Point out each leukocyte.
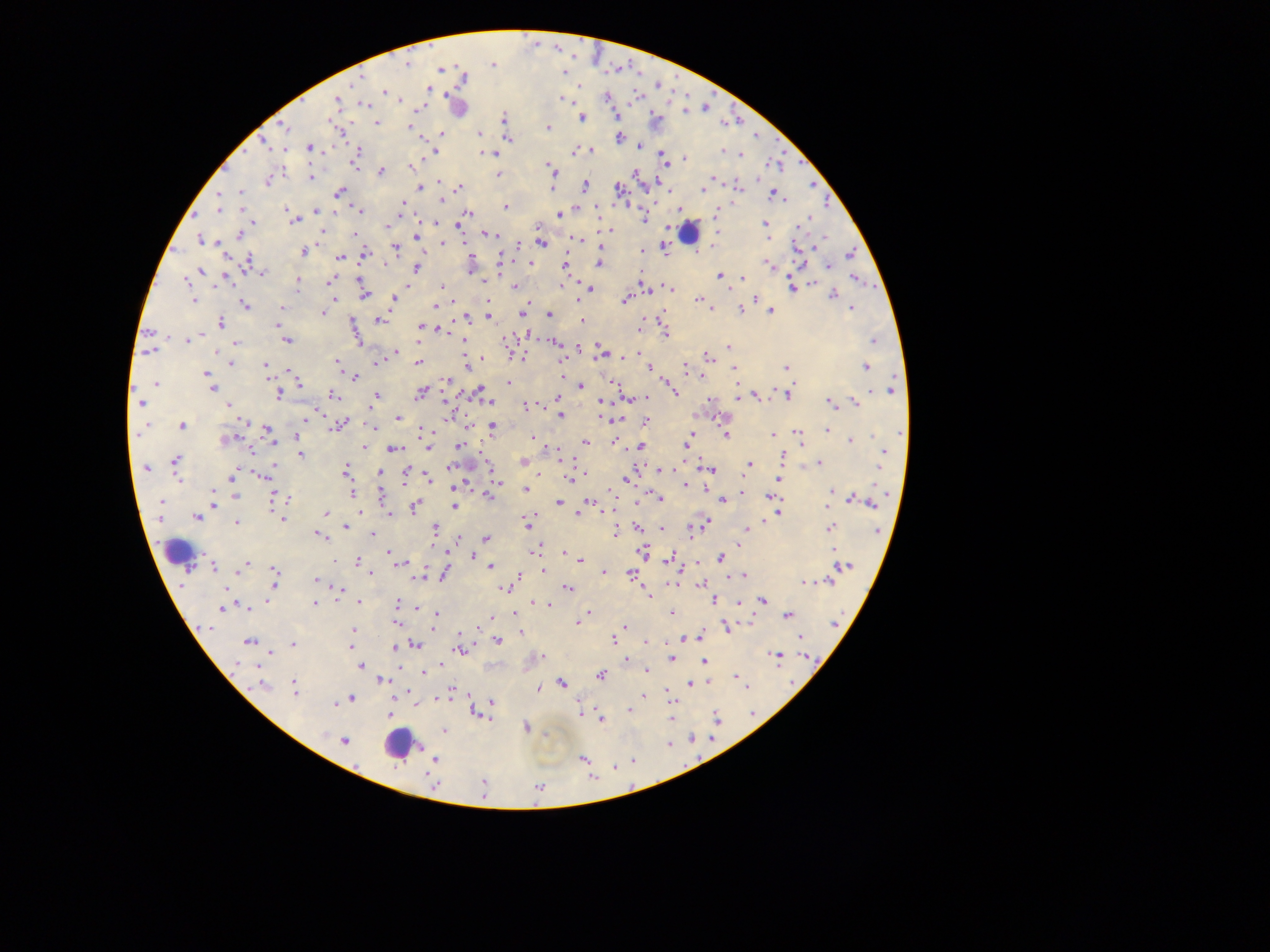

Approximate centers as {x, y} in pixels.
Leukocytes: {457, 106}, {688, 232}, {470, 462}, {178, 552}, {400, 744}.

Plasmodium parasite locations: {406, 62}, {493, 62}, {441, 68}, {564, 69}, {358, 77}, {428, 89}, {384, 91}, {566, 97}, {607, 97}, {642, 97}, {398, 100}, {337, 101}, {363, 104}, {684, 109}, {615, 116}, {503, 118}, {582, 118}, {328, 121}, {377, 122}, {409, 126}, {286, 128}, {548, 128}, {442, 134}, {479, 134}, {618, 138}, {508, 139}, {263, 142}, {640, 146}, {309, 147}, {358, 151}, {575, 151}, {590, 151}, {723, 151}, {434, 152}, {740, 153}, {493, 154}, {685, 158}, {663, 159}, {665, 163}, {355, 164}, {548, 165}, {551, 169}, {381, 171}, {497, 175}, {311, 177}, {267, 181}, {441, 182}, {813, 185}, {585, 186}, {737, 187}, {419, 188}, {459, 188}, {552, 188}, {619, 189}, {704, 190}, {240, 191}, {340, 192}, {776, 195}, {442, 200}, {401, 204}, {505, 207}, {220, 209}, {578, 209}, {316, 211}, {361, 211}, {715, 212}, {466, 214}, {560, 214}, {290, 215}, {464, 219}, {644, 219}, {294, 220}, {802, 223}, {458, 224}, {765, 224}, {387, 226}, {606, 230}, {321, 231}, {353, 233}, {239, 235}, {492, 235}, {417, 236}, {769, 238}, {201, 239}, {574, 240}, {466, 241}, {443, 243}, {520, 243}, {542, 243}, {601, 246}, {396, 249}, {665, 249}, {642, 251}, {303, 252}, {363, 254}, {850, 254}, {339, 257}, {248, 262}, {600, 263}, {530, 264}, {770, 264}, {564, 265}, {828, 266}, {417, 267}, {201, 271}, {469, 271}, {261, 273}, {720, 274}, {640, 277}, {743, 278}, {224, 279}, {856, 279}, {186, 281}, {330, 281}, {297, 282}, {359, 282}, {812, 284}, {217, 285}, {515, 286}, {562, 286}, {791, 286}, {407, 287}, {441, 287}, {643, 287}, {669, 288}, {590, 289}, {833, 294}, {364, 295}, {335, 299}, {393, 299}, {698, 299}, {756, 299}, {193, 300}, {625, 301}, {245, 305}, {435, 306}, {283, 308}, {709, 308}, {852, 309}, {741, 310}, {770, 311}, {323, 314}, {522, 314}, {549, 315}, {488, 316}, {469, 317}, {663, 318}, {380, 321}, {582, 321}, {220, 323}, {277, 325}, {420, 326}, {640, 327}, {440, 331}, {355, 333}, {666, 334}, {202, 336}, {462, 339}, {187, 340}, {286, 340}, {874, 340}, {235, 343}, {556, 343}, {503, 347}, {728, 347}, {578, 348}, {150, 351}, {217, 352}, {395, 352}, {603, 352}, {639, 352}, {633, 355}, {522, 357}, {707, 358}, {482, 359}, {418, 362}, {377, 363}, {231, 364}, {336, 364}, {264, 365}, {466, 366}, {646, 366}, {685, 367}, {786, 367}, {866, 367}, {650, 368}, {734, 368}, {266, 370}, {291, 370}, {206, 374}, {208, 378}, {354, 378}, {446, 380}, {613, 382}, {299, 383}, {509, 383}, {156, 384}, {581, 385}, {737, 386}, {212, 387}, {673, 388}, {892, 390}, {479, 391}, {675, 391}, {420, 393}, {332, 395}, {787, 395}, {279, 396}, {376, 396}, {756, 396}, {645, 397}, {558, 398}, {738, 398}, {490, 402}, {830, 402}, {855, 402}, {140, 403}, {228, 405}, {525, 405}, {370, 408}, {560, 415}, {311, 416}, {397, 418}, {241, 421}, {646, 423}, {182, 426}, {339, 426}, {492, 427}, {372, 428}, {268, 430}, {423, 430}, {827, 431}, {902, 432}, {138, 433}, {692, 433}, {798, 433}, {726, 435}, {773, 435}, {297, 437}, {229, 439}, {533, 439}, {272, 440}, {851, 440}, {535, 441}, {614, 441}, {585, 442}, {688, 444}, {363, 446}, {429, 447}, {458, 447}, {641, 447}, {394, 450}, {251, 452}, {883, 452}, {300, 454}, {782, 457}, {175, 461}, {749, 464}, {819, 464}, {450, 467}, {146, 468}, {879, 468}, {272, 470}, {345, 470}, {660, 470}, {712, 470}, {235, 472}, {379, 472}, {585, 473}, {406, 474}, {264, 476}, {177, 477}, {233, 477}, {569, 478}, {778, 478}, {430, 479}, {627, 479}, {496, 480}, {685, 485}, {455, 488}, {526, 489}, {235, 491}, {832, 491}, {213, 492}, {743, 493}, {352, 494}, {771, 495}, {235, 496}, {382, 496}, {488, 496}, {273, 498}, {660, 498}, {855, 499}, {288, 500}, {722, 500}, {161, 501}, {866, 501}, {590, 503}, {559, 504}, {214, 505}, {454, 506}, {414, 507}, {579, 511}, {360, 512}, {327, 513}, {389, 513}, {778, 513}, {196, 517}, {282, 519}, {768, 520}, {705, 522}, {527, 524}, {234, 525}, {346, 527}, {830, 527}, {639, 528}, {748, 528}, {436, 529}, {663, 529}, {694, 530}, {615, 532}, {318, 534}, {372, 534}, {486, 538}, {458, 541}, {536, 551}, {387, 552}, {643, 552}, {564, 553}, {473, 556}, {721, 557}, {670, 558}, {580, 560}, {357, 562}, {397, 563}, {213, 565}, {490, 566}, {844, 566}, {245, 567}, {542, 570}, {605, 572}, {371, 573}, {444, 573}, {630, 573}, {275, 574}, {742, 576}, {419, 577}, {316, 580}, {829, 581}, {805, 584}, {701, 585}, {504, 587}, {568, 588}, {338, 589}, {648, 594}, {714, 600}, {762, 600}, {360, 602}, {535, 603}, {739, 603}, {314, 604}, {397, 604}, {549, 605}, {248, 607}, {418, 608}, {221, 609}, {589, 613}, {672, 613}, {436, 614}, {515, 614}, {788, 616}, {396, 623}, {578, 623}, {433, 626}, {624, 627}, {726, 627}, {208, 628}, {353, 630}, {521, 632}, {460, 633}, {699, 637}, {801, 637}, {498, 640}, {613, 640}, {248, 641}, {647, 642}, {415, 644}, {293, 645}, {351, 648}, {394, 648}, {461, 651}, {270, 652}, {777, 657}, {672, 658}, {626, 659}, {705, 662}, {237, 664}, {361, 666}, {647, 671}, {423, 673}, {601, 675}, {737, 678}, {381, 680}, {562, 683}, {690, 683}, {262, 685}, {746, 687}, {538, 689}, {295, 690}, {450, 691}, {643, 695}, {351, 699}, {342, 701}, {491, 703}, {336, 704}, {629, 710}, {580, 713}, {390, 715}, {671, 717}, {716, 718}, {601, 719}, {526, 727}, {444, 731}, {344, 741}, {435, 759}, {582, 759}. Collected in Ghana. Image is 1270×952 pixels. Photographed through a microscope with a mobile-phone camera. One field of view. Thick blood smear.